Point out each leukocyte.
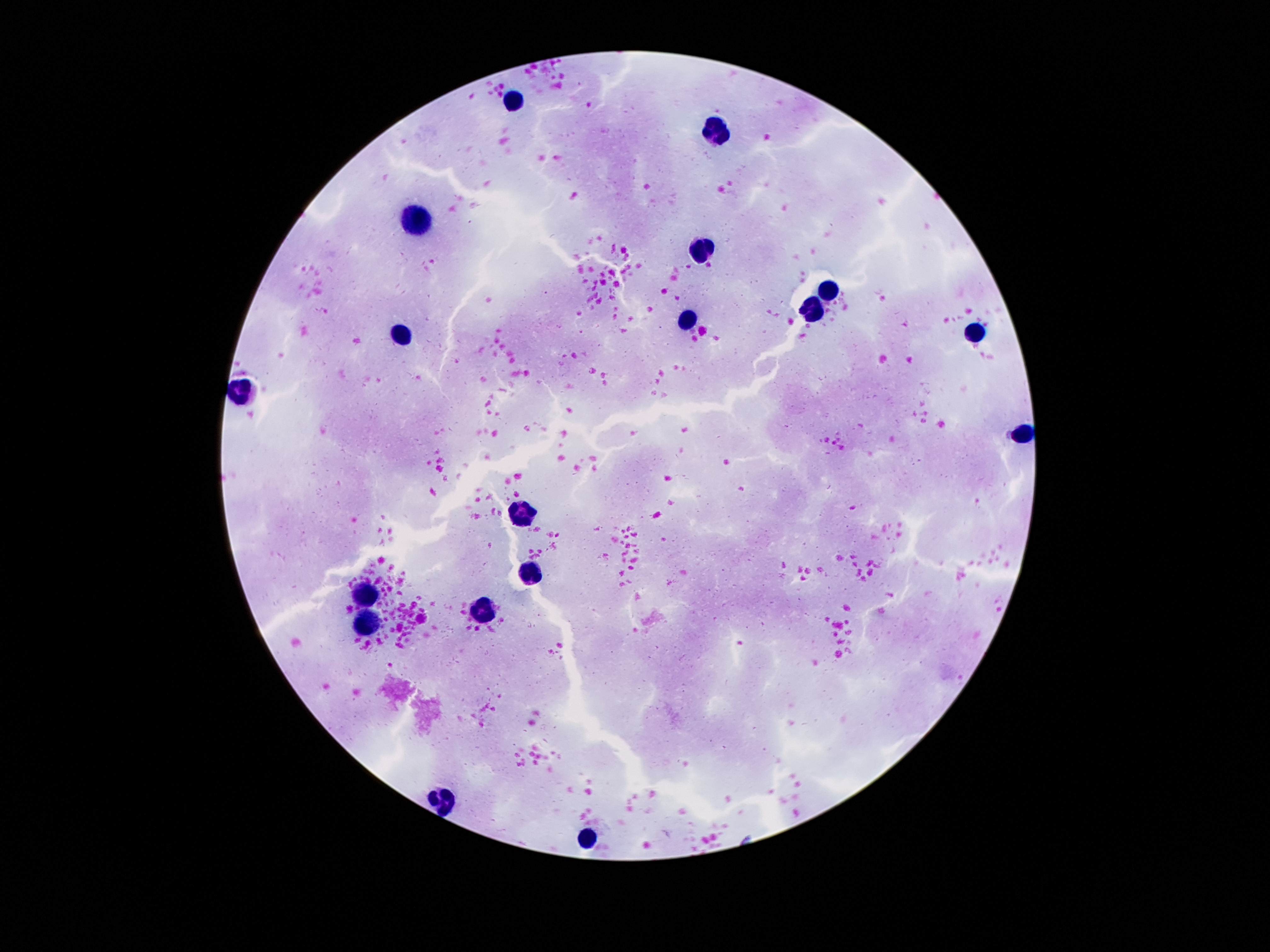
Approximate object centers, in pixels from the top-left corner.
Leukocytes: (x=514, y=99), (x=717, y=132), (x=417, y=226), (x=699, y=249), (x=828, y=290), (x=813, y=308), (x=687, y=322), (x=976, y=332), (x=399, y=336), (x=241, y=393), (x=1024, y=432), (x=522, y=513), (x=532, y=574), (x=367, y=594), (x=484, y=612), (x=372, y=623), (x=441, y=801), (x=589, y=841).

field of view = single
stain = Giemsa
patient malaria status = uninfected
preparation = thick blood smear
capture = smartphone camera through the microscope eyepiece
magnification = 100x
image size = 1270×952 pixels